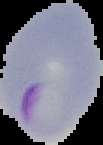

Summary:
  - Image type: cell region segmented out of the field of view; surrounding area masked to black
  - Preparation: thin blood smear
  - Result: Plasmodium parasites identified
  - Image size: 103×145 pixels